Comment on the morphology of the erythrocytes.
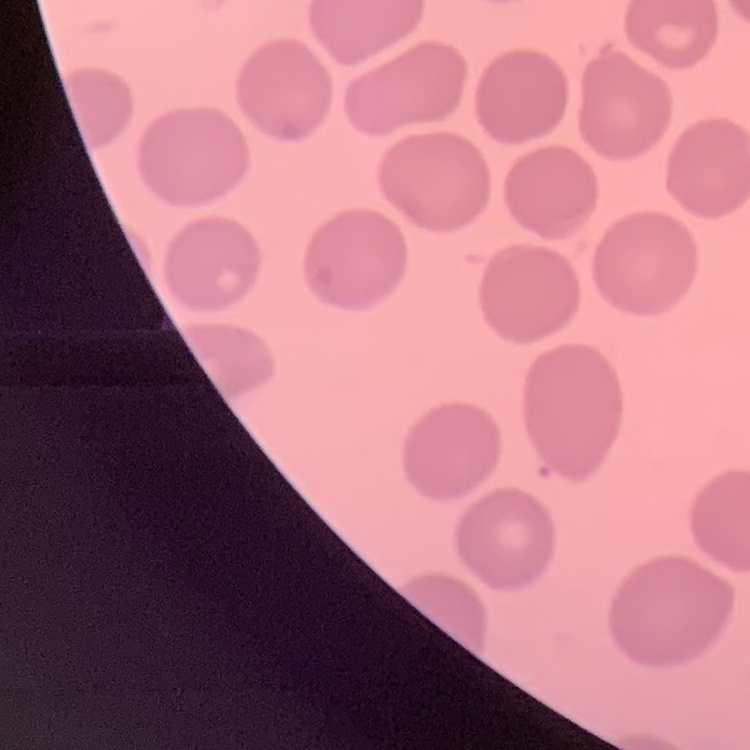

No rouleaux formation.

stain = Field's or Giemsa
preparation = thin peripheral smear
image type = one tile cut from a larger photomicrograph